Report the malaria status of this cell.
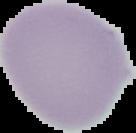
It is uninfected.

From a thin blood film. The area outside the segmented cell region is set to black. Image is 136×133 pixels.